Evaluate for parasitized red blood cells.
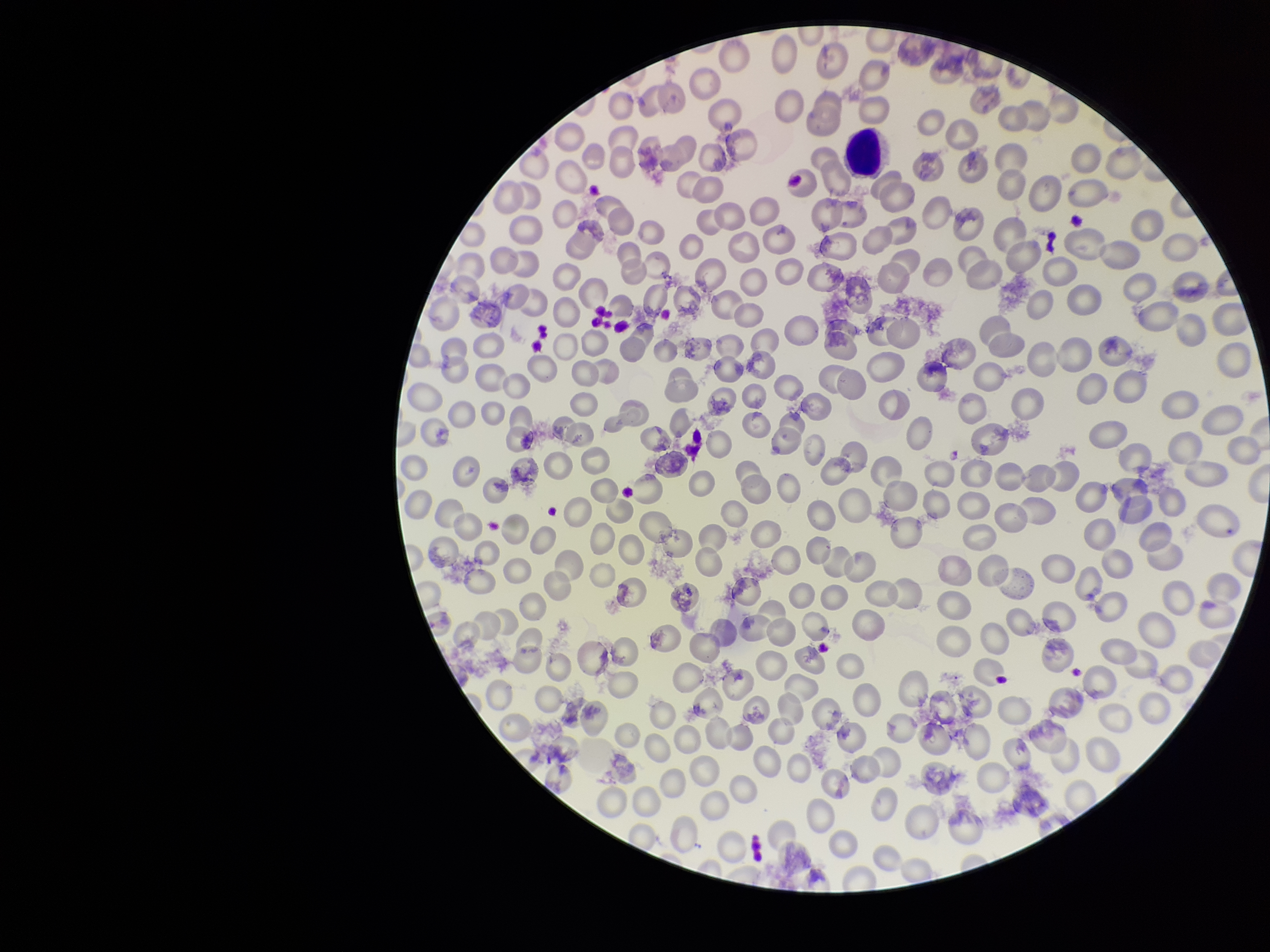

None identified.

Giemsa stain. Smartphone photograph taken through the eyepiece of a microscope. Image is 1270×952 pixels. One field from this slide. Red blood cell count: 253. Preparation: thin blood smear. Patient malaria status: negative. Parasitized red blood cell count: 0.